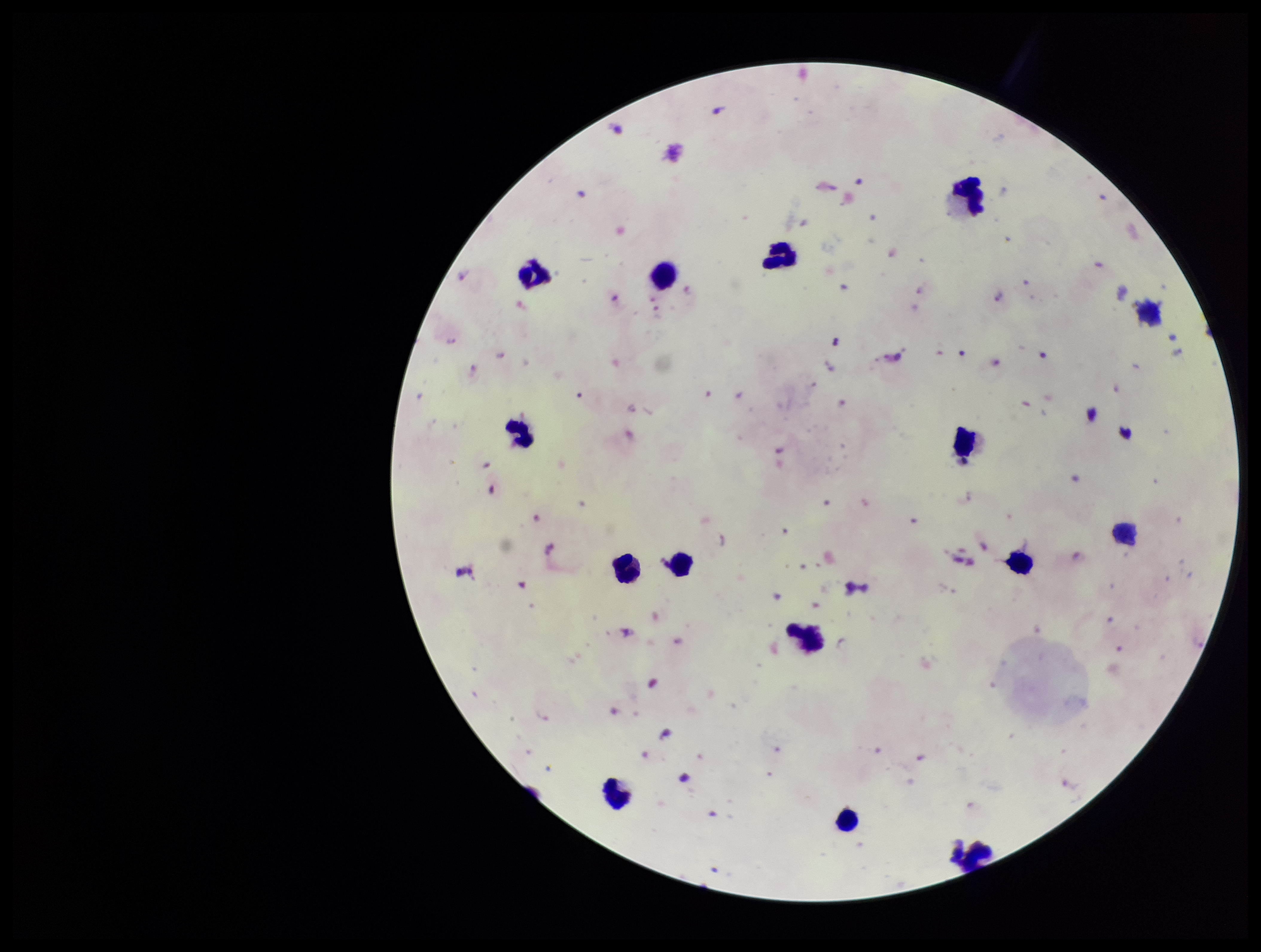
Summary:
  - Parasite count: 29
  - Stain: Giemsa
  - Leukocyte count: 14
  - Field of view: one from this slide
  - Preparation: thick
  - Species reported for this patient: Plasmodium falciparum
  - Patient malaria status: infected
  - Image size: 1261×952 pixels
  - Plasmodium parasites: seen
  - Capture: smartphone photograph through the microscope eyepiece